Classify this cell by malaria status.
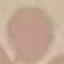

It is uninfected.

Acquired by smartphone through the microscope eyepiece. Giemsa stain. Cell patch, automatically extracted from a larger field of view and resized to 64 × 64 pixels. Thin blood film.